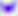

identification: Toxoplasma gondii
modality: micrograph
magnification: 400x